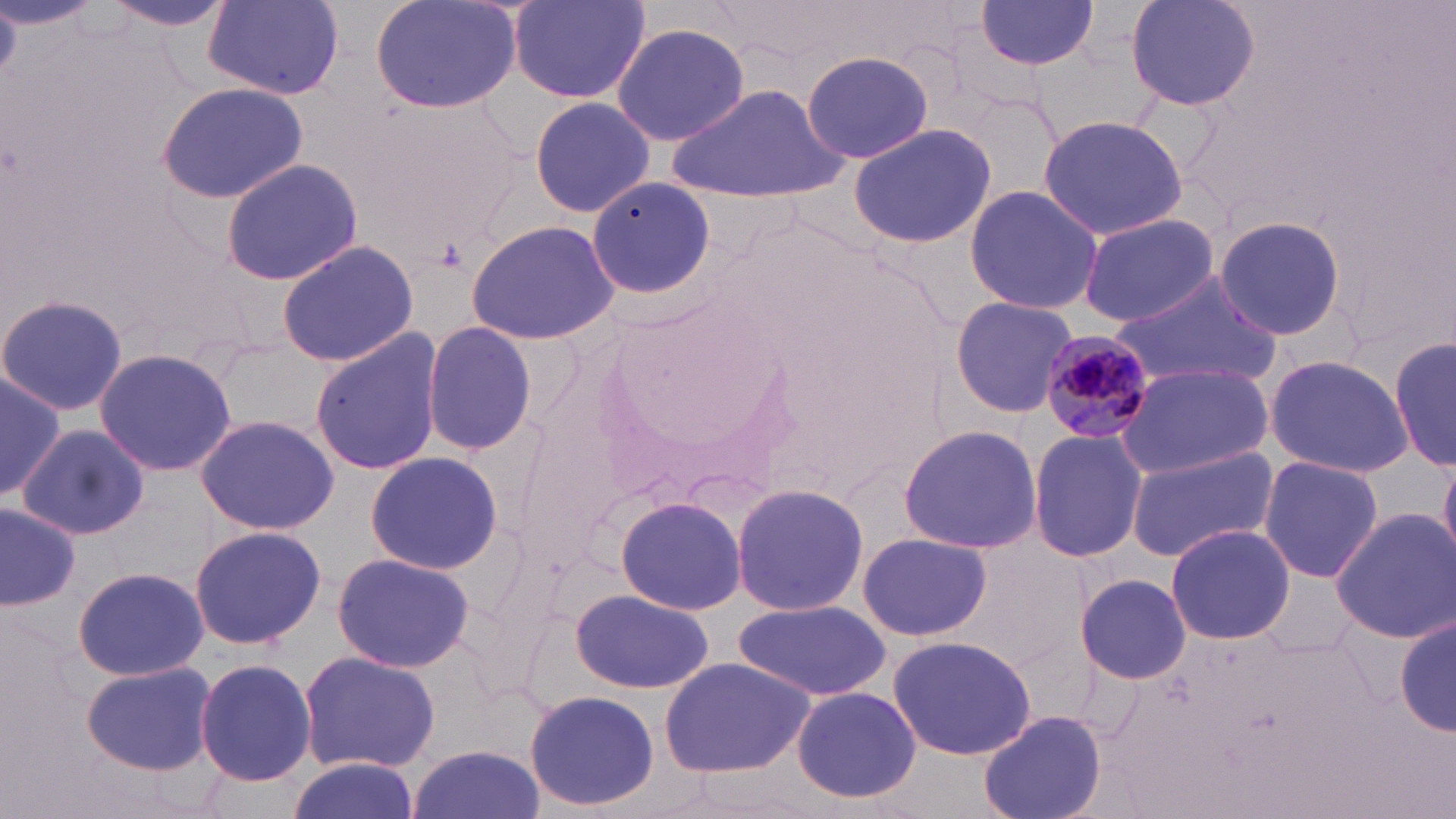
slide-level diagnosis = Plasmodium malariae
image size = 1456×819 pixels
field of view = one of a larger specimen
Plasmodium malariae-infected red blood cell locations = approximate bounding boxes as named x1/y1/x2/y2 corners in pixels: (x1=1041, y1=332, x2=1151, y2=442)
uninfected red blood cell locations = approximate bounding boxes as named x1/y1/x2/y2 corners in pixels: (x1=370, y1=0, x2=523, y2=115), (x1=1125, y1=0, x2=1259, y2=113), (x1=104, y1=1, x2=234, y2=34), (x1=507, y1=1, x2=650, y2=103), (x1=974, y1=1, x2=1102, y2=70), (x1=204, y1=2, x2=345, y2=97), (x1=610, y1=21, x2=749, y2=147), (x1=802, y1=48, x2=934, y2=165), (x1=157, y1=83, x2=305, y2=204), (x1=674, y1=84, x2=845, y2=202), (x1=528, y1=95, x2=656, y2=216), (x1=1036, y1=115, x2=1190, y2=240), (x1=846, y1=123, x2=998, y2=247), (x1=220, y1=159, x2=364, y2=287), (x1=586, y1=175, x2=717, y2=304), (x1=963, y1=185, x2=1103, y2=316), (x1=1078, y1=213, x2=1221, y2=326), (x1=1212, y1=213, x2=1349, y2=342), (x1=467, y1=219, x2=622, y2=346), (x1=276, y1=239, x2=419, y2=367), (x1=1110, y1=274, x2=1281, y2=384), (x1=0, y1=292, x2=129, y2=419), (x1=948, y1=297, x2=1078, y2=416), (x1=421, y1=321, x2=540, y2=458), (x1=308, y1=329, x2=445, y2=476), (x1=1390, y1=336, x2=1454, y2=473), (x1=94, y1=347, x2=237, y2=477), (x1=1264, y1=353, x2=1414, y2=478), (x1=1117, y1=363, x2=1272, y2=479), (x1=0, y1=366, x2=63, y2=506), (x1=194, y1=413, x2=338, y2=534), (x1=896, y1=423, x2=1043, y2=554), (x1=17, y1=425, x2=150, y2=540), (x1=1027, y1=426, x2=1147, y2=563), (x1=1124, y1=444, x2=1280, y2=563), (x1=364, y1=451, x2=505, y2=576), (x1=1439, y1=454, x2=1456, y2=561), (x1=1257, y1=455, x2=1385, y2=583), (x1=730, y1=481, x2=872, y2=619), (x1=615, y1=496, x2=746, y2=615), (x1=0, y1=502, x2=80, y2=609), (x1=1330, y1=507, x2=1455, y2=643), (x1=1165, y1=524, x2=1295, y2=644), (x1=188, y1=526, x2=327, y2=649), (x1=858, y1=532, x2=991, y2=641), (x1=332, y1=552, x2=476, y2=673), (x1=72, y1=565, x2=209, y2=681), (x1=1069, y1=571, x2=1195, y2=684), (x1=571, y1=587, x2=715, y2=695), (x1=734, y1=599, x2=890, y2=702), (x1=1393, y1=612, x2=1454, y2=739), (x1=888, y1=635, x2=1038, y2=760), (x1=297, y1=650, x2=441, y2=774), (x1=195, y1=657, x2=317, y2=788), (x1=659, y1=657, x2=817, y2=778), (x1=81, y1=659, x2=218, y2=776), (x1=792, y1=687, x2=923, y2=805), (x1=522, y1=689, x2=661, y2=812), (x1=979, y1=711, x2=1107, y2=819), (x1=407, y1=744, x2=546, y2=819), (x1=283, y1=758, x2=420, y2=819)
magnification = 1000x
stain = May-Grünwald-Giemsa
modality = light microscopy
preparation = thin blood smear